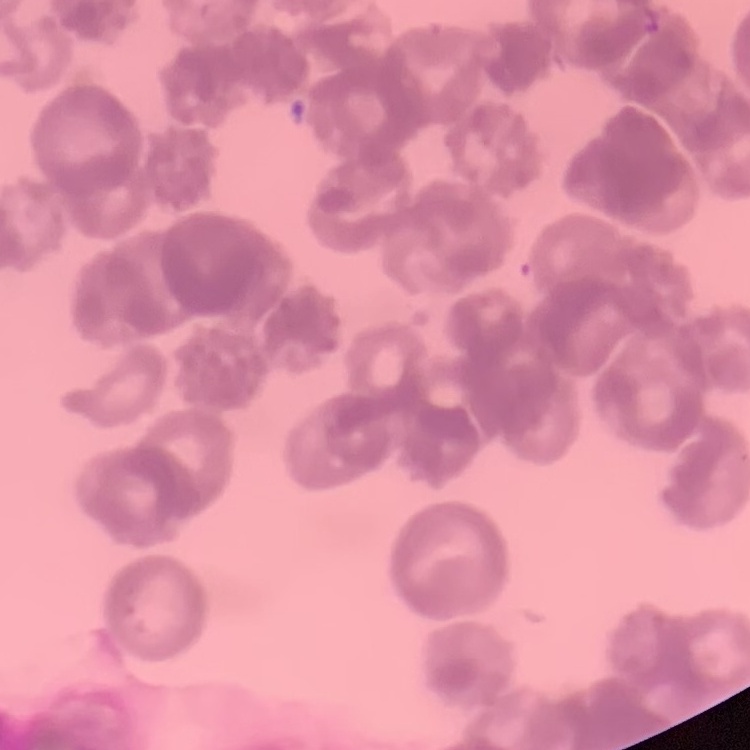

Summary:
  - Red blood cell morphology: rouleaux formation
  - Preparation: thin blood smear
  - Stain: Field's or Giemsa
  - Image type: one tile cut from a larger photomicrograph